Assess this cell for malaria.
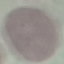

It is uninfected.

capture = smartphone camera at the microscope eyepiece
image type = automatically extracted cell patch, resized to 64 × 64 pixels
stain = Giemsa
preparation = thin blood smear